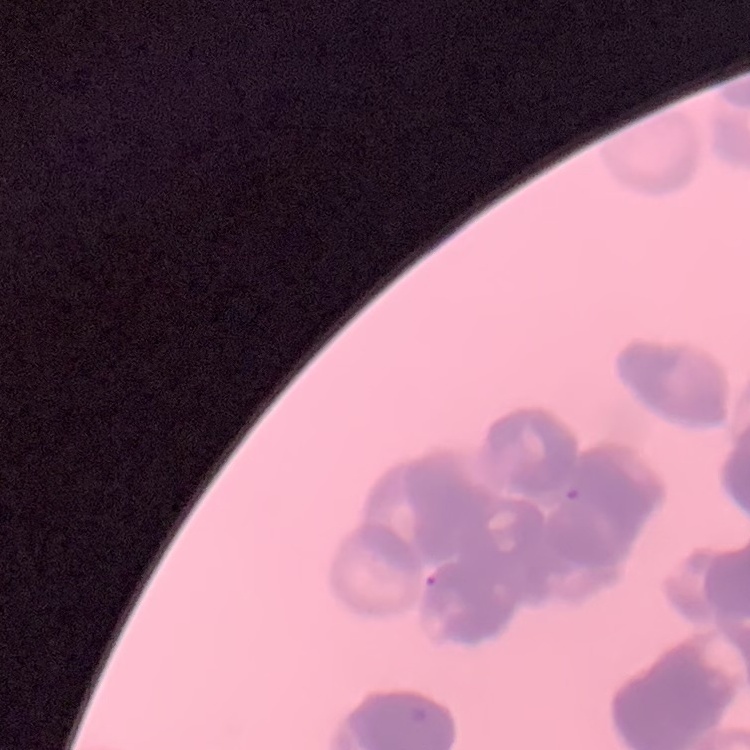

erythrocyte morphology = rouleaux formation
preparation = thin blood smear
image type = one tile cut from a larger photomicrograph
stain = Field's or Giemsa